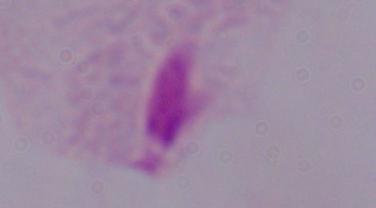

Photomicrograph. A trichomonad is shown. Captured at 1000x magnification.